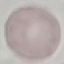
Malaria status: uninfected. Thin smear of blood. Acquired by smartphone through the microscope eyepiece. Giemsa-stained preparation. Automatically extracted cell patch, resized to 64 × 64 pixels.